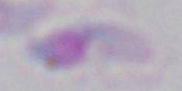
identification = Toxoplasma gondii
modality = micrograph
magnification = 1000x